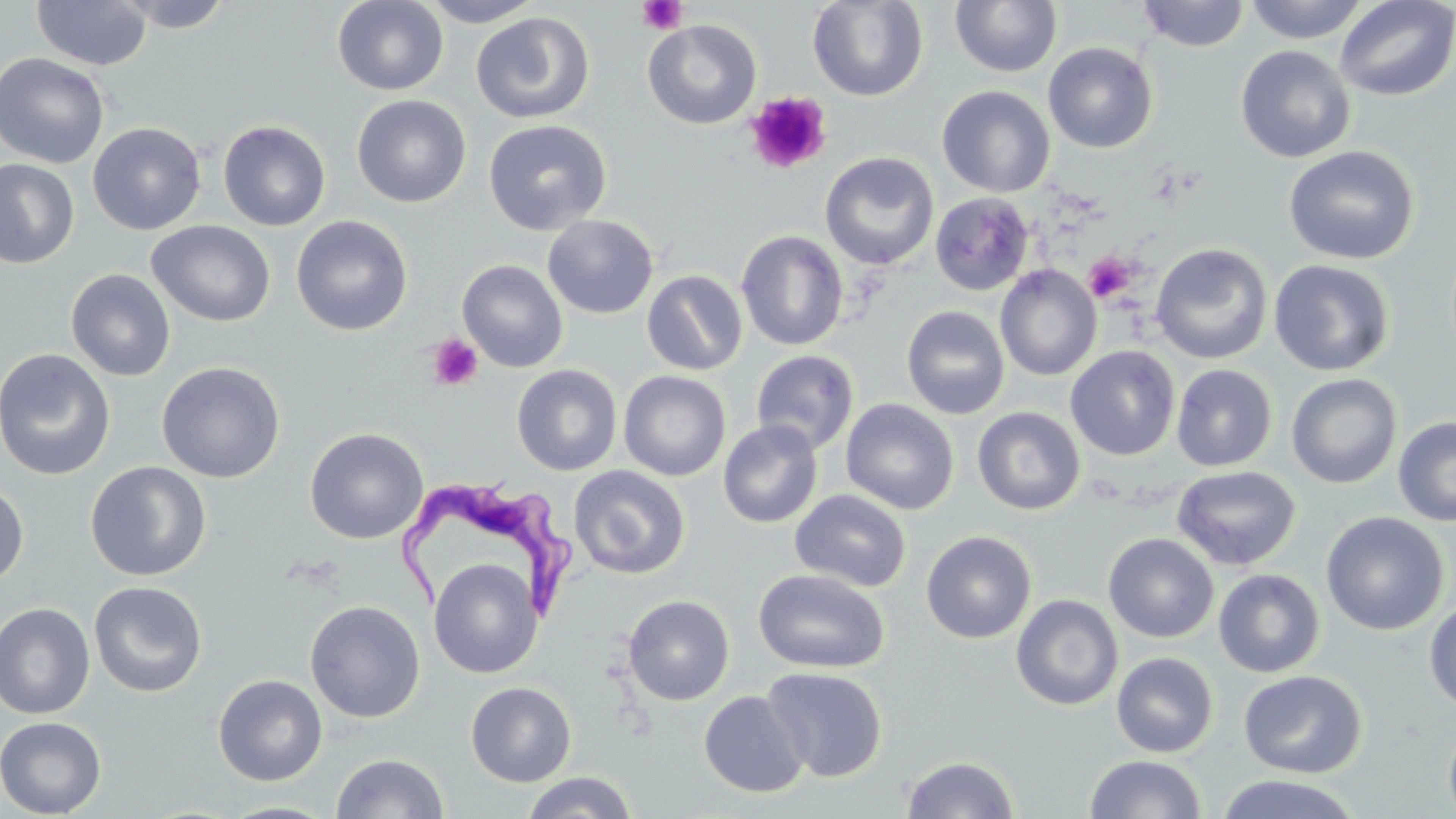

Approximate bounding boxes as named x1/y1/x2/y2 corners in pixels. Uninfected red blood cell locations: (x1=113, y1=0, x2=237, y2=32), (x1=332, y1=0, x2=449, y2=95), (x1=417, y1=0, x2=546, y2=27), (x1=807, y1=0, x2=929, y2=101), (x1=949, y1=0, x2=1062, y2=77), (x1=1242, y1=0, x2=1372, y2=43), (x1=1334, y1=0, x2=1456, y2=102), (x1=31, y1=1, x2=152, y2=70), (x1=1136, y1=1, x2=1252, y2=52), (x1=470, y1=12, x2=595, y2=124), (x1=642, y1=19, x2=762, y2=129), (x1=1043, y1=42, x2=1158, y2=153), (x1=1234, y1=45, x2=1356, y2=163), (x1=0, y1=52, x2=110, y2=169), (x1=936, y1=85, x2=1055, y2=198), (x1=351, y1=95, x2=472, y2=207), (x1=218, y1=119, x2=331, y2=231), (x1=484, y1=119, x2=612, y2=235), (x1=87, y1=122, x2=206, y2=235), (x1=1282, y1=145, x2=1420, y2=265), (x1=819, y1=152, x2=939, y2=271), (x1=0, y1=159, x2=80, y2=269), (x1=929, y1=192, x2=1034, y2=295), (x1=542, y1=214, x2=658, y2=319), (x1=291, y1=215, x2=413, y2=336), (x1=147, y1=220, x2=276, y2=327), (x1=736, y1=230, x2=849, y2=351), (x1=1151, y1=243, x2=1273, y2=365), (x1=457, y1=259, x2=568, y2=372), (x1=1268, y1=259, x2=1395, y2=376), (x1=995, y1=265, x2=1102, y2=380), (x1=65, y1=268, x2=176, y2=381), (x1=642, y1=269, x2=748, y2=376), (x1=901, y1=305, x2=1011, y2=419), (x1=1065, y1=345, x2=1180, y2=461), (x1=0, y1=347, x2=115, y2=480), (x1=750, y1=349, x2=859, y2=456), (x1=156, y1=361, x2=285, y2=483), (x1=512, y1=364, x2=622, y2=476), (x1=1171, y1=364, x2=1278, y2=472), (x1=619, y1=370, x2=731, y2=481), (x1=1286, y1=373, x2=1402, y2=489), (x1=840, y1=398, x2=959, y2=515), (x1=972, y1=406, x2=1086, y2=515), (x1=1393, y1=416, x2=1456, y2=526), (x1=718, y1=420, x2=823, y2=528), (x1=304, y1=427, x2=428, y2=544), (x1=85, y1=461, x2=211, y2=580), (x1=568, y1=465, x2=691, y2=579), (x1=1172, y1=465, x2=1302, y2=570), (x1=0, y1=479, x2=29, y2=588), (x1=790, y1=489, x2=911, y2=593), (x1=1320, y1=511, x2=1449, y2=635), (x1=921, y1=530, x2=1036, y2=644), (x1=1103, y1=533, x2=1219, y2=643), (x1=429, y1=558, x2=543, y2=678), (x1=752, y1=568, x2=890, y2=674), (x1=1213, y1=569, x2=1326, y2=678), (x1=89, y1=581, x2=208, y2=697), (x1=1011, y1=594, x2=1123, y2=710), (x1=622, y1=595, x2=735, y2=706), (x1=304, y1=600, x2=425, y2=723), (x1=1423, y1=600, x2=1456, y2=712), (x1=0, y1=602, x2=96, y2=719), (x1=1111, y1=652, x2=1218, y2=758), (x1=762, y1=667, x2=888, y2=782), (x1=1239, y1=669, x2=1367, y2=778), (x1=213, y1=674, x2=327, y2=786), (x1=465, y1=682, x2=576, y2=786), (x1=698, y1=690, x2=809, y2=798), (x1=1443, y1=715, x2=1456, y2=819), (x1=0, y1=717, x2=107, y2=818), (x1=331, y1=752, x2=448, y2=819), (x1=900, y1=754, x2=1020, y2=818), (x1=1084, y1=754, x2=1207, y2=818), (x1=521, y1=771, x2=638, y2=819), (x1=1211, y1=773, x2=1366, y2=819), (x1=216, y1=800, x2=341, y2=819). Platelet locations: (x1=637, y1=0, x2=688, y2=34), (x1=744, y1=92, x2=831, y2=174), (x1=1083, y1=252, x2=1138, y2=303), (x1=427, y1=334, x2=484, y2=390). Trypanosoma brucei locations: (x1=391, y1=474, x2=580, y2=623). Slide-level diagnosis: Trypanosoma brucei. Optical microscopy. Image is 1456×819 pixels. Thin blood smear. One field of a larger specimen. 1000x magnification. May-Grünwald-Giemsa stain.